Locate every blood parasite and identify its species.
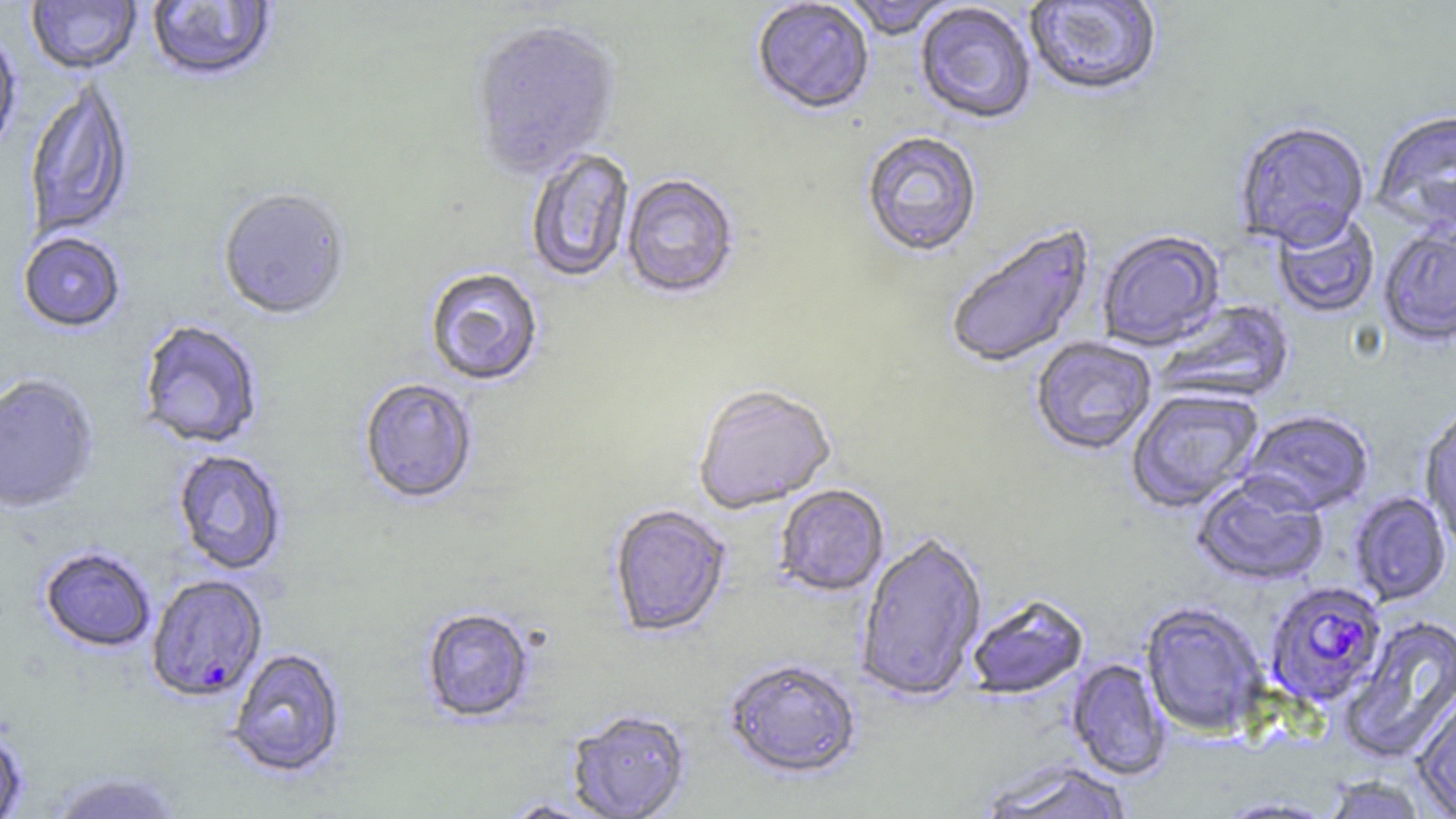

Approximate bounding boxes as [x1, y1, x2, y2] in pixels.
Plasmodium falciparum-infected red blood cells: [145, 575, 268, 703], [1264, 581, 1387, 707].
No Plasmodium ovale, Plasmodium malariae, Plasmodium vivax, Babesia divergens, or Trypanosoma brucei observed.

{
  "slide_level_diagnosis": "Plasmodium falciparum",
  "stain": "May-Grünwald-Giemsa",
  "image_size": "1456×819 pixels",
  "magnification": "1000x",
  "preparation": "thin blood smear",
  "field_of_view": "single",
  "modality": "light microscopy",
  "uninfected_red_blood_cell_locations": "approximate bounding boxes as [x1, y1, x2, y2] in pixels: [27, 0, 141, 76], [146, 0, 278, 86], [841, 0, 958, 41], [1024, 0, 1163, 99], [752, 1, 874, 118], [915, 3, 1036, 126], [470, 23, 621, 182], [0, 31, 21, 161], [24, 78, 135, 241], [1371, 111, 1456, 235], [1233, 122, 1370, 250], [861, 131, 983, 259], [525, 149, 635, 284], [621, 175, 740, 302], [218, 191, 350, 322], [1272, 212, 1379, 319], [944, 222, 1095, 371], [1378, 225, 1456, 349], [1097, 231, 1225, 350], [18, 232, 126, 334], [424, 268, 544, 387], [1153, 299, 1296, 406], [137, 320, 265, 451], [1031, 337, 1156, 456], [0, 374, 100, 514], [358, 379, 478, 506], [692, 386, 836, 515], [1126, 388, 1265, 513], [1420, 406, 1456, 547], [1240, 410, 1376, 516], [172, 450, 288, 576], [1191, 474, 1329, 587], [774, 486, 889, 598], [1349, 492, 1451, 606], [608, 504, 732, 639], [856, 534, 988, 703], [39, 547, 155, 653], [966, 594, 1089, 700], [1139, 601, 1269, 737], [421, 608, 535, 724], [1339, 615, 1456, 765], [227, 648, 347, 778], [1067, 658, 1171, 780], [723, 659, 862, 781], [1412, 692, 1456, 817], [566, 709, 691, 819], [0, 727, 29, 819], [976, 760, 1135, 819], [45, 769, 187, 818], [1321, 775, 1429, 819], [1215, 796, 1339, 818]"
}